Name the parasite shown.
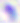

This is Toxoplasma gondii.

{
  "modality": "photomicrograph",
  "magnification": "400x"
}